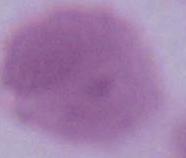

identification = erythrocyte
magnification = 1000x
modality = micrograph